State the blood parasite species.
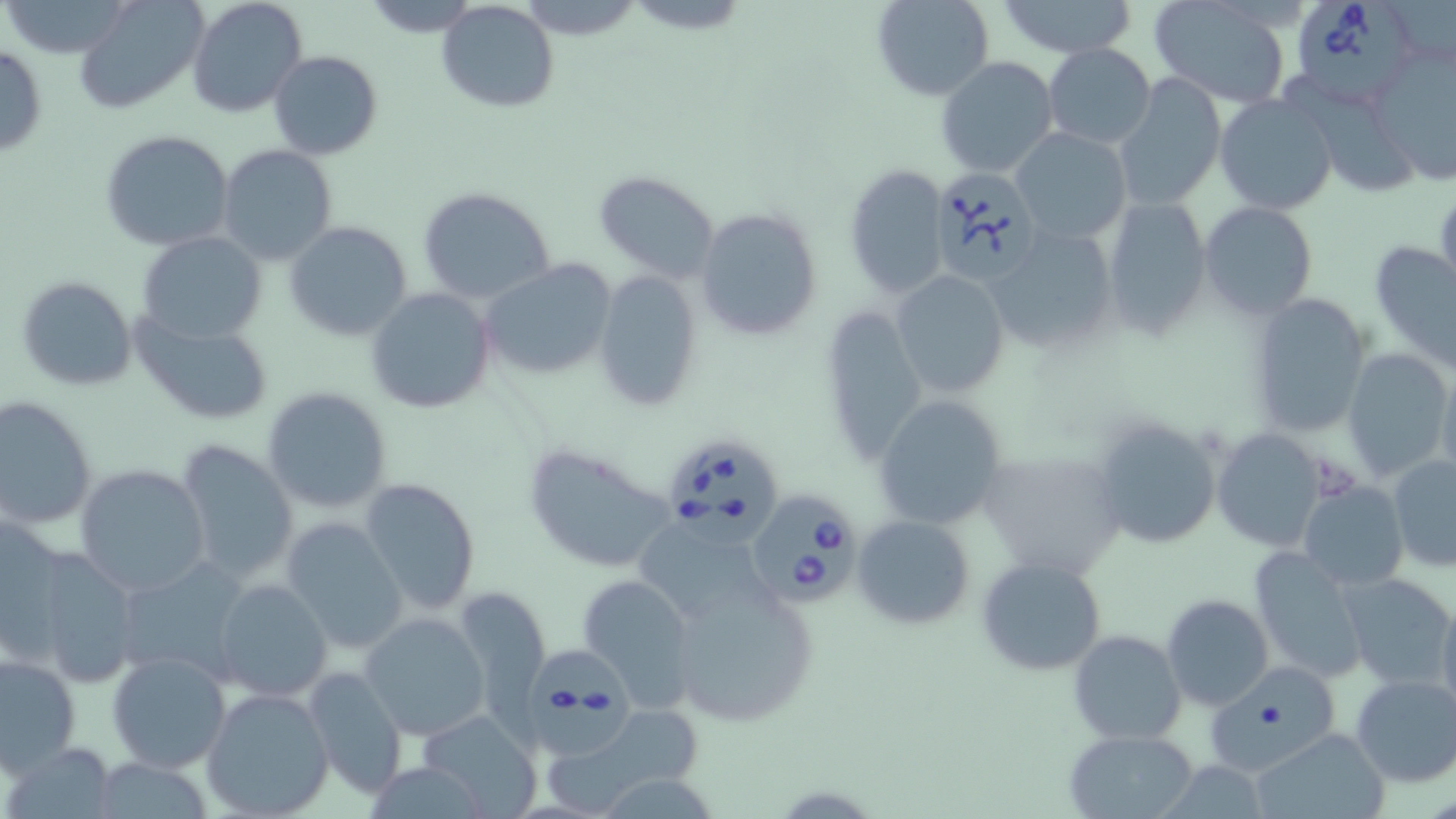
Babesia divergens.

Summary:
  - Coordinate format: approximate bounding boxes as named x1/y1/x2/y2 corners in pixels
  - Uninfected red blood cell locations: (x1=0, y1=0, x2=136, y2=57), (x1=74, y1=0, x2=208, y2=115), (x1=187, y1=0, x2=307, y2=117), (x1=436, y1=0, x2=559, y2=114), (x1=870, y1=0, x2=996, y2=103), (x1=991, y1=0, x2=1141, y2=57), (x1=356, y1=1, x2=485, y2=35), (x1=1149, y1=2, x2=1291, y2=107), (x1=1042, y1=42, x2=1157, y2=151), (x1=0, y1=44, x2=47, y2=158), (x1=1369, y1=45, x2=1456, y2=186), (x1=268, y1=51, x2=382, y2=159), (x1=936, y1=56, x2=1059, y2=178), (x1=1116, y1=74, x2=1225, y2=208), (x1=1283, y1=75, x2=1416, y2=200), (x1=1213, y1=92, x2=1338, y2=217), (x1=1011, y1=128, x2=1132, y2=242), (x1=100, y1=129, x2=235, y2=251), (x1=218, y1=146, x2=337, y2=264), (x1=844, y1=164, x2=951, y2=302), (x1=593, y1=172, x2=721, y2=283), (x1=417, y1=186, x2=557, y2=306), (x1=1434, y1=187, x2=1456, y2=299), (x1=1100, y1=197, x2=1212, y2=341), (x1=1199, y1=202, x2=1318, y2=320), (x1=693, y1=207, x2=822, y2=340), (x1=284, y1=220, x2=414, y2=342), (x1=984, y1=226, x2=1119, y2=356), (x1=137, y1=232, x2=266, y2=343), (x1=1369, y1=240, x2=1456, y2=371), (x1=480, y1=258, x2=617, y2=379), (x1=592, y1=270, x2=702, y2=412), (x1=891, y1=270, x2=1010, y2=398), (x1=15, y1=274, x2=138, y2=392), (x1=365, y1=288, x2=496, y2=414), (x1=1247, y1=292, x2=1371, y2=439), (x1=815, y1=306, x2=927, y2=464), (x1=134, y1=314, x2=271, y2=424), (x1=1342, y1=347, x2=1453, y2=484), (x1=1435, y1=363, x2=1456, y2=488), (x1=261, y1=387, x2=393, y2=514), (x1=0, y1=396, x2=98, y2=531), (x1=871, y1=396, x2=1006, y2=529), (x1=1089, y1=414, x2=1224, y2=552), (x1=1211, y1=429, x2=1328, y2=551), (x1=177, y1=439, x2=298, y2=585), (x1=521, y1=440, x2=682, y2=575), (x1=977, y1=447, x2=1125, y2=579), (x1=1388, y1=453, x2=1456, y2=571), (x1=75, y1=465, x2=210, y2=596), (x1=359, y1=478, x2=484, y2=618), (x1=1297, y1=480, x2=1408, y2=592), (x1=1, y1=513, x2=68, y2=648), (x1=852, y1=515, x2=975, y2=629), (x1=281, y1=518, x2=407, y2=653), (x1=638, y1=523, x2=755, y2=618), (x1=13, y1=544, x2=143, y2=685), (x1=1249, y1=544, x2=1371, y2=685), (x1=976, y1=556, x2=1107, y2=675), (x1=114, y1=557, x2=251, y2=683), (x1=576, y1=573, x2=698, y2=706), (x1=1337, y1=574, x2=1454, y2=691), (x1=212, y1=578, x2=334, y2=702), (x1=672, y1=585, x2=816, y2=729), (x1=450, y1=586, x2=552, y2=722), (x1=1435, y1=591, x2=1456, y2=724), (x1=1160, y1=594, x2=1273, y2=711), (x1=359, y1=612, x2=490, y2=742), (x1=1068, y1=629, x2=1186, y2=744), (x1=107, y1=650, x2=232, y2=772), (x1=0, y1=652, x2=81, y2=776), (x1=1200, y1=662, x2=1342, y2=775), (x1=302, y1=665, x2=407, y2=801), (x1=1350, y1=674, x2=1456, y2=788), (x1=201, y1=687, x2=335, y2=818), (x1=580, y1=705, x2=703, y2=796), (x1=420, y1=712, x2=543, y2=813), (x1=1251, y1=727, x2=1390, y2=819), (x1=1065, y1=729, x2=1201, y2=817), (x1=3, y1=741, x2=118, y2=817), (x1=88, y1=757, x2=218, y2=816)
  - Babesia divergens-infected red blood cell locations: (x1=1299, y1=1, x2=1414, y2=105), (x1=928, y1=165, x2=1044, y2=285), (x1=672, y1=444, x2=784, y2=550), (x1=741, y1=492, x2=861, y2=602), (x1=521, y1=648, x2=638, y2=761)
  - Magnification: 1000x
  - Modality: light microscopy
  - Field of view: one of a larger specimen
  - Preparation: thin blood smear
  - Image size: 1456×819 pixels
  - Stain: May-Grünwald-Giemsa